Locate every blood parasite and identify its species.
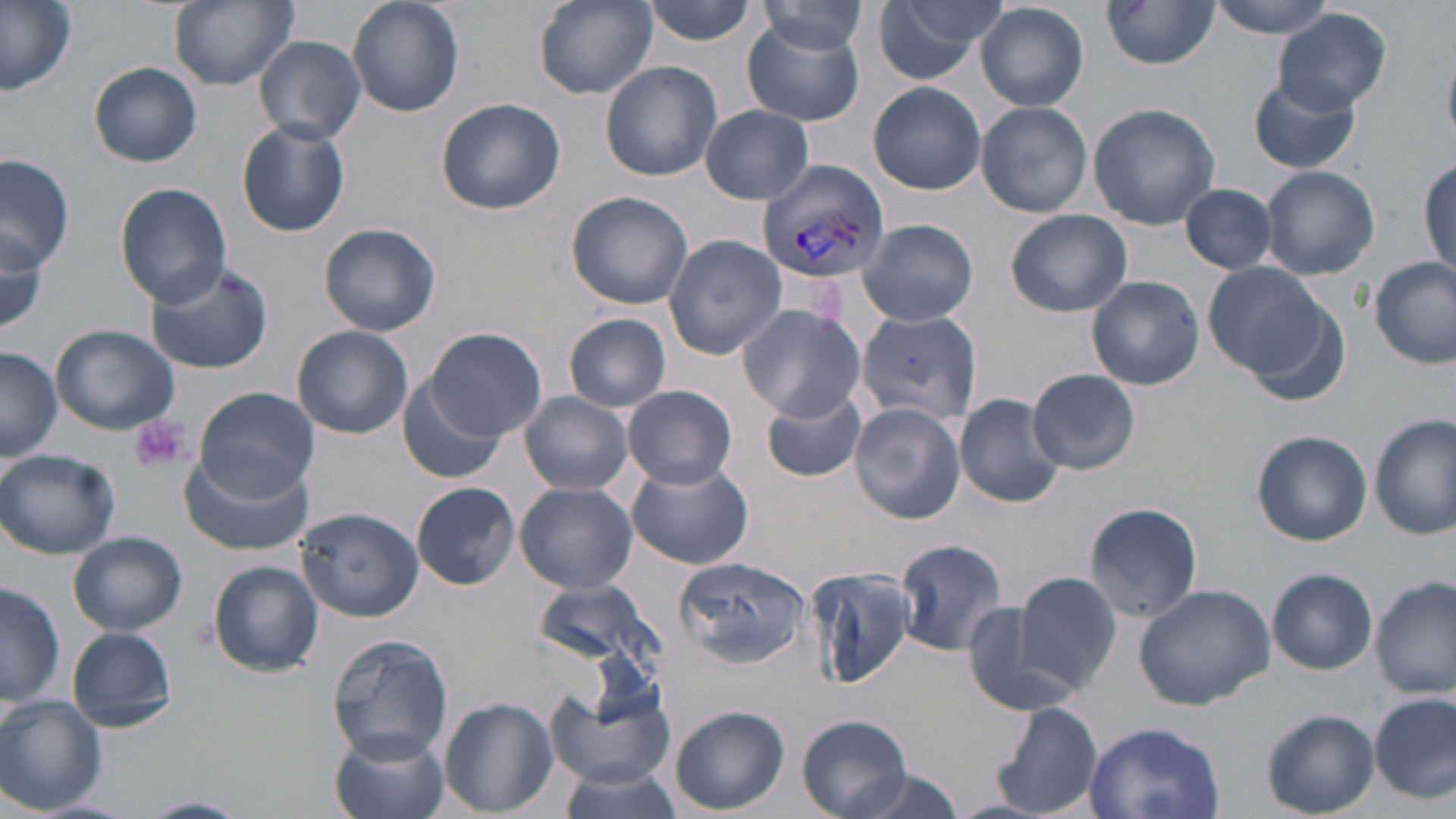

Approximate bounding boxes as (x1,y1)-(x2,y2) corner pairs in pixels.
Plasmodium vivax-infected red blood cells: (756,158)-(889,285).
No Plasmodium falciparum, Plasmodium ovale, Plasmodium malariae, Babesia divergens, or Trypanosoma brucei observed.

slide-level diagnosis = Plasmodium vivax
stain = May-Grünwald-Giemsa
field of view = one of a larger specimen
modality = optical microscopy
platelet locations = approximate bounding boxes as (x1,y1)-(x2,y2) corner pairs in pixels: (129,414)-(191,474)
preparation = thin blood film
uninfected red blood cell locations = approximate bounding boxes as (x1,y1)-(x2,y2) corner pairs in pixels: (0,0)-(77,99), (170,0)-(297,89), (347,0)-(462,117), (534,0)-(657,99), (871,0)-(1007,86), (1204,0)-(1340,36), (641,1)-(762,46), (756,3)-(869,54), (1100,3)-(1219,70), (975,4)-(1088,110), (1276,9)-(1391,115), (741,16)-(868,127), (254,35)-(365,148), (600,60)-(723,180), (89,62)-(202,167), (1249,76)-(1362,175), (868,80)-(988,194), (436,98)-(567,215), (975,102)-(1093,217), (1088,102)-(1221,229), (699,104)-(814,204), (237,120)-(350,236), (0,154)-(74,273), (1418,155)-(1456,281), (1259,165)-(1380,279), (116,184)-(231,306), (1182,185)-(1278,273), (566,191)-(694,311), (1005,209)-(1133,317), (856,218)-(979,328), (319,222)-(441,336), (0,223)-(47,340), (662,233)-(786,359), (1370,255)-(1455,367), (144,258)-(276,374), (1203,261)-(1327,380), (1087,275)-(1204,390), (735,302)-(866,423), (857,309)-(983,429), (565,312)-(670,413), (51,326)-(179,434), (293,326)-(414,438), (425,329)-(546,439), (0,346)-(63,461), (1028,369)-(1141,473), (400,378)-(506,485), (623,385)-(738,489), (760,385)-(868,482), (194,386)-(319,501), (518,392)-(633,494), (955,392)-(1065,508), (850,402)-(965,523), (1372,414)-(1454,539), (1251,430)-(1373,547), (0,448)-(121,559), (180,452)-(313,556), (624,460)-(754,570), (514,481)-(638,595), (412,482)-(518,589), (1083,502)-(1205,623), (296,507)-(423,622), (69,533)-(187,636), (893,537)-(1010,655), (675,555)-(810,666), (209,561)-(325,676), (805,565)-(917,689), (1266,568)-(1377,673), (1014,573)-(1122,694), (1373,576)-(1454,698), (531,580)-(664,676), (1,581)-(63,709), (1133,582)-(1276,711), (960,596)-(1074,717), (66,626)-(177,732), (327,634)-(453,763), (17,660)-(126,775), (543,673)-(680,791), (1371,693)-(1455,803), (0,696)-(107,814), (440,697)-(558,818), (990,701)-(1104,817), (671,706)-(788,815), (1261,709)-(1379,817), (797,714)-(914,819), (1081,720)-(1227,818), (330,727)-(450,819), (556,765)-(687,818), (842,767)-(969,819), (135,796)-(250,819)
image size = 1456×819 pixels
magnification = 1000x